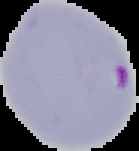

{
  "result": "Plasmodium parasites identified",
  "preparation": "thin blood film",
  "image_size": "139×151 pixels",
  "image_type": "segmented cell region on a black background"
}